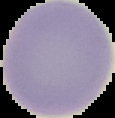

image_type: segmented cell region with the area outside set to black
image_size: 115×118 pixels
result: no malaria parasites detected
preparation: thin blood film